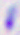

magnification = 400x
modality = photomicrograph
identification = Toxoplasma gondii